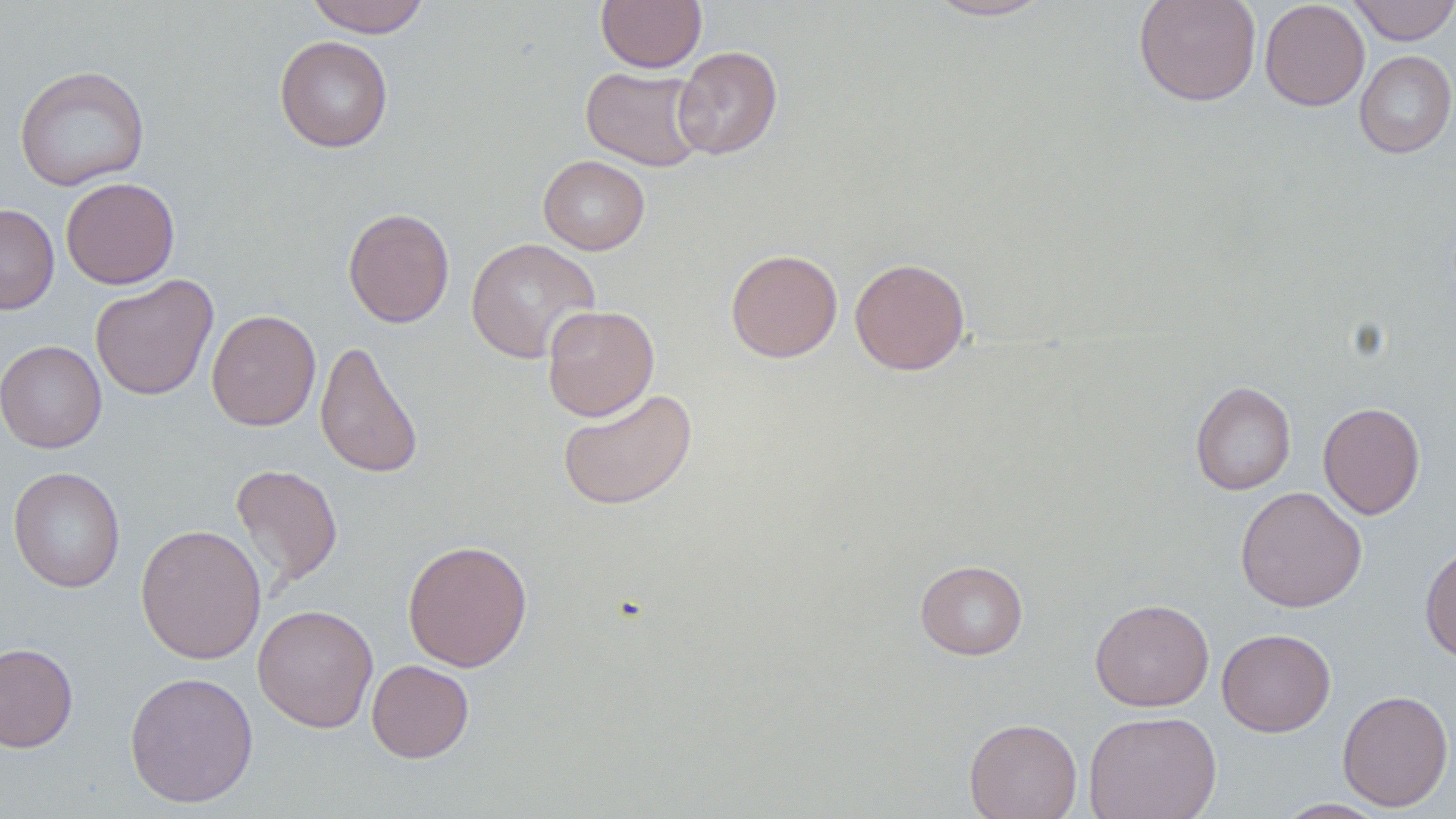
slide-level diagnosis = negative for blood parasites
modality = optical microscopy
magnification = 1000x
uninfected red blood cell locations = approximate bounding boxes as named x1/y1/x2/y2 corners in pixels: (x1=304, y1=0, x2=431, y2=37), (x1=596, y1=0, x2=707, y2=72), (x1=925, y1=0, x2=1055, y2=21), (x1=1133, y1=0, x2=1261, y2=106), (x1=1260, y1=0, x2=1370, y2=111), (x1=1347, y1=0, x2=1456, y2=45), (x1=274, y1=36, x2=393, y2=152), (x1=672, y1=46, x2=782, y2=159), (x1=1354, y1=50, x2=1456, y2=158), (x1=14, y1=65, x2=150, y2=191), (x1=581, y1=67, x2=707, y2=171), (x1=538, y1=155, x2=650, y2=255), (x1=61, y1=177, x2=180, y2=289), (x1=0, y1=203, x2=60, y2=315), (x1=343, y1=207, x2=455, y2=328), (x1=465, y1=237, x2=601, y2=363), (x1=725, y1=248, x2=843, y2=363), (x1=850, y1=258, x2=970, y2=375), (x1=90, y1=274, x2=218, y2=401), (x1=541, y1=304, x2=659, y2=421), (x1=206, y1=309, x2=321, y2=432), (x1=315, y1=339, x2=424, y2=479), (x1=0, y1=340, x2=107, y2=453), (x1=1190, y1=381, x2=1296, y2=495), (x1=558, y1=388, x2=697, y2=510), (x1=1318, y1=402, x2=1425, y2=520), (x1=230, y1=464, x2=343, y2=589), (x1=8, y1=467, x2=125, y2=593), (x1=1235, y1=486, x2=1367, y2=612), (x1=135, y1=523, x2=267, y2=665), (x1=402, y1=539, x2=532, y2=672), (x1=1420, y1=542, x2=1456, y2=664), (x1=915, y1=559, x2=1028, y2=660), (x1=1090, y1=597, x2=1214, y2=712), (x1=253, y1=604, x2=379, y2=732), (x1=1217, y1=628, x2=1336, y2=736), (x1=0, y1=643, x2=78, y2=753), (x1=366, y1=659, x2=474, y2=763), (x1=124, y1=670, x2=258, y2=808), (x1=1337, y1=689, x2=1454, y2=812), (x1=1083, y1=710, x2=1222, y2=819), (x1=964, y1=718, x2=1082, y2=819), (x1=1274, y1=798, x2=1391, y2=818)
image size = 1456×819 pixels
stain = May-Grünwald-Giemsa
preparation = thin blood smear
field of view = one of a larger specimen